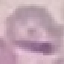

Summary:
  - Result: no malaria parasites seen
  - Image type: automatically extracted cell patch, resized to 64 × 64 pixels
  - Preparation: thin smear
  - Capture: smartphone camera at the microscope eyepiece
  - Stain: Giemsa